Evaluate for malaria.
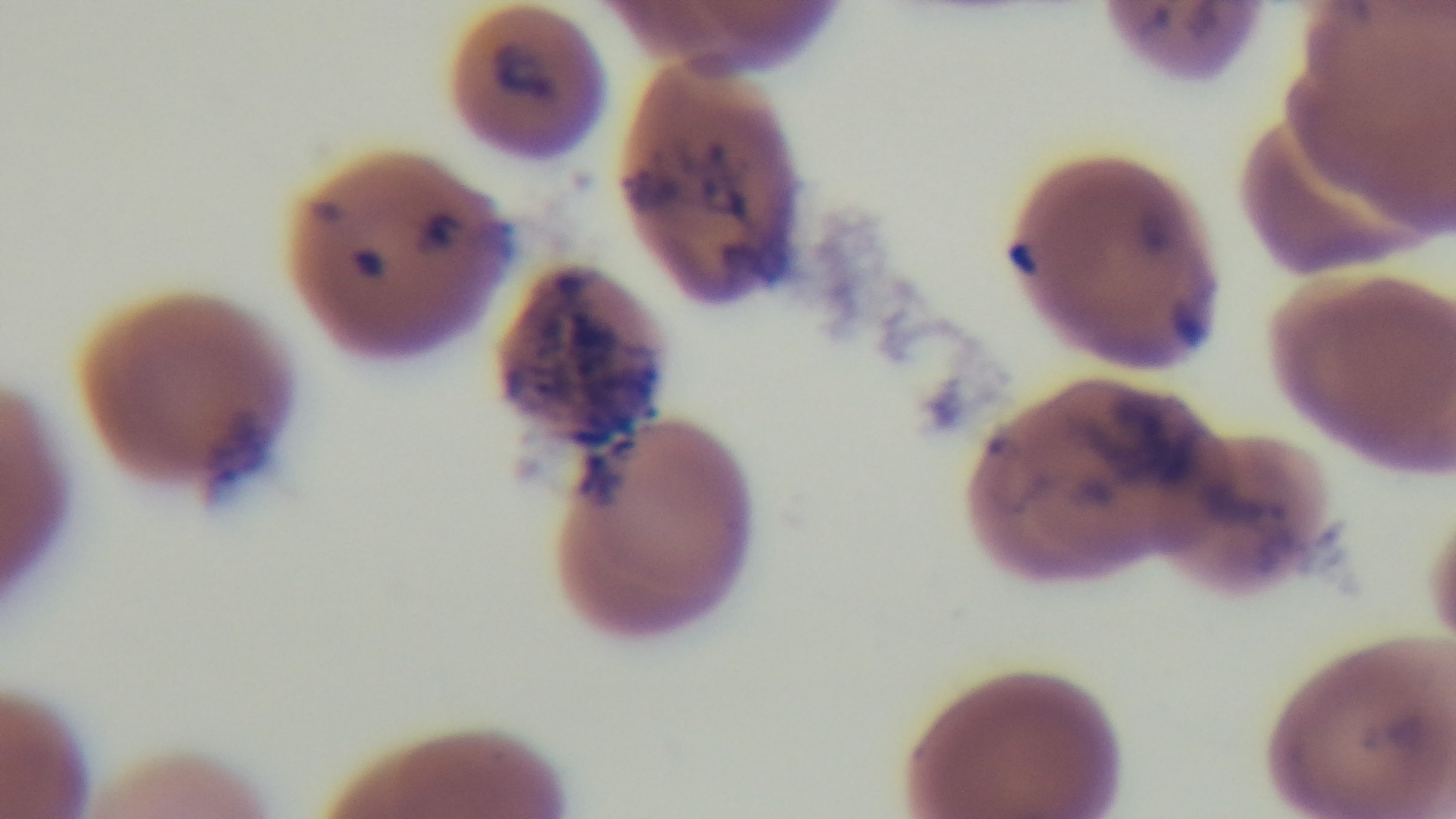
It is infected.

Light microscopy. One field from the slide. Mounted 4K digital camera. Oil-immersion objective, 100x. Preparation: thin smear. Giemsa stain.